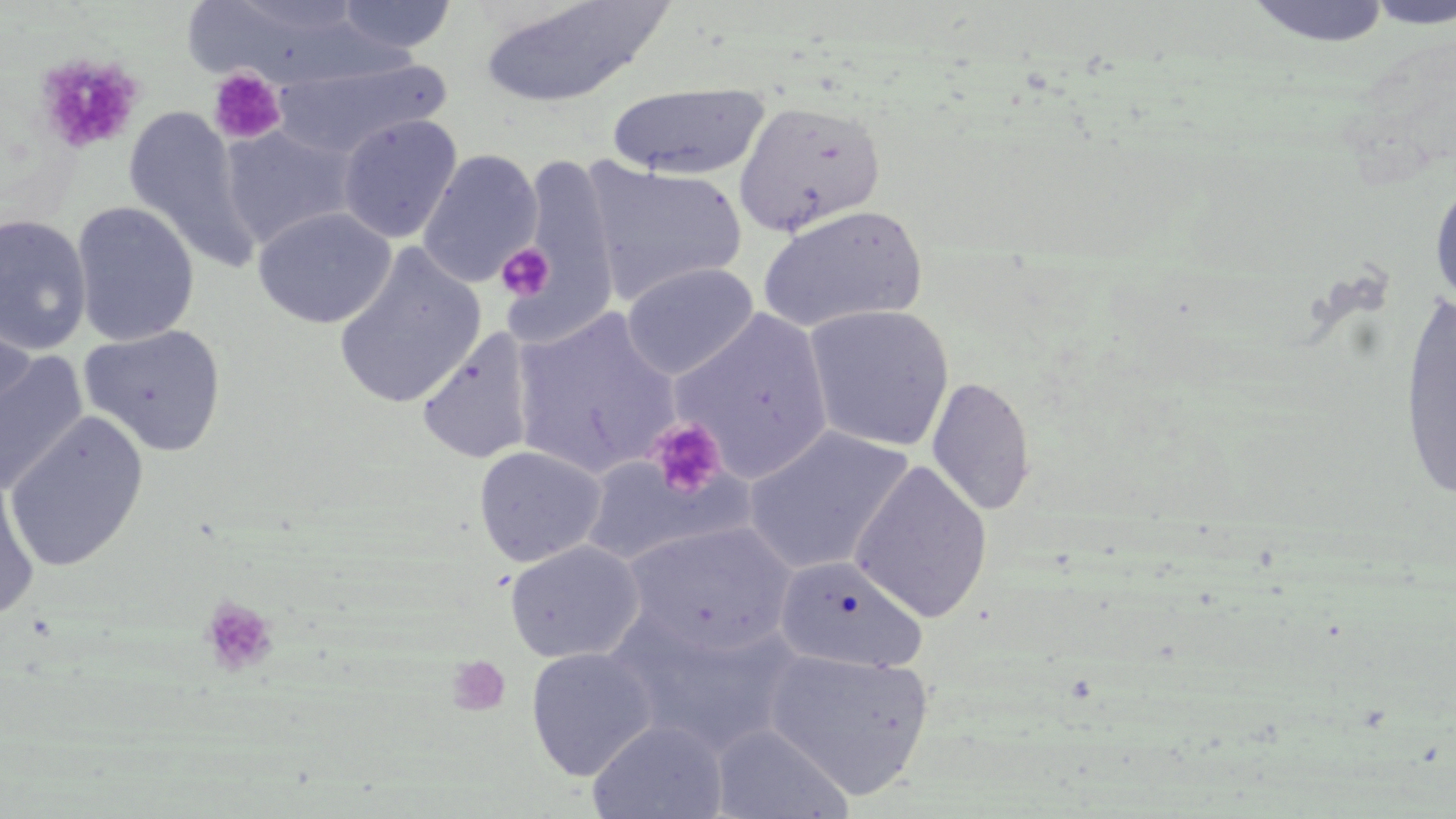

Summary:
  - Coordinate format: approximate bounding boxes as (x1,y1)-(x2,y2) corner pairs in pixels
  - Platelet locations: (36,52)-(143,155), (208,68)-(286,145), (496,243)-(555,302), (646,417)-(727,500), (199,596)-(278,677), (447,655)-(512,717)
  - Uninfected red blood cell locations: (334,0)-(458,54), (476,0)-(674,110), (1244,0)-(1393,51), (1360,3)-(1456,31), (270,55)-(451,159), (606,83)-(770,180), (733,99)-(888,238), (123,106)-(256,270), (338,114)-(462,244), (220,123)-(359,250), (417,149)-(543,288), (515,151)-(621,344), (584,162)-(748,304), (1429,175)-(1456,311), (71,201)-(200,347), (757,205)-(928,334), (254,206)-(395,329), (0,214)-(93,355), (333,244)-(487,410), (621,262)-(759,379), (1397,289)-(1455,504), (802,304)-(954,451), (510,309)-(681,477), (671,309)-(833,481), (0,318)-(37,432), (79,324)-(227,457), (417,329)-(537,465), (0,349)-(89,497), (926,375)-(1036,517), (3,411)-(150,572), (742,427)-(913,576), (474,445)-(607,567), (580,455)-(736,568), (850,460)-(993,623), (0,474)-(41,622), (624,521)-(795,656), (505,540)-(645,663), (774,555)-(928,675), (613,615)-(801,757), (525,647)-(659,780), (763,648)-(935,799), (587,719)-(729,819), (711,723)-(853,818)
  - Slide-level diagnosis: negative for blood parasites
  - Image size: 1456×819 pixels
  - Field of view: one of a larger specimen
  - Modality: light microscopy
  - Preparation: thin blood film
  - Stain: May-Grünwald-Giemsa
  - Magnification: 1000x